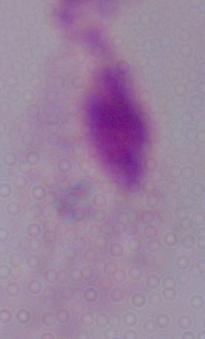
modality = photomicrograph
identification = trichomonad
magnification = 1000x